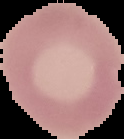
From a thin blood smear. Image is 124×139 pixels. Malaria status: uninfected. The area outside the segmented cell region is set to black.